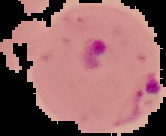
Summary:
  - Image size: 166×136 pixels
  - Image type: segmented cell region with the area outside set to black
  - Malaria status: parasitized
  - Preparation: thin blood film